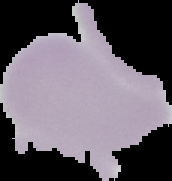 Image is 172×181 pixels. The area outside the segmented cell region is set to black. From a thin blood film. Malaria status: uninfected.